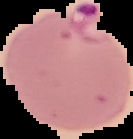 Malaria status: parasitized. From a thin blood film. Image is 133×139 pixels. Cell region segmented out of the field of view; the surrounding area is masked to black.